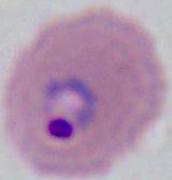 Photomicrograph. 400x or 1000x magnification. A Plasmodium parasite is seen.